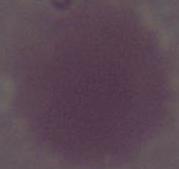

modality: micrograph
identification: erythrocyte
magnification: 1000x